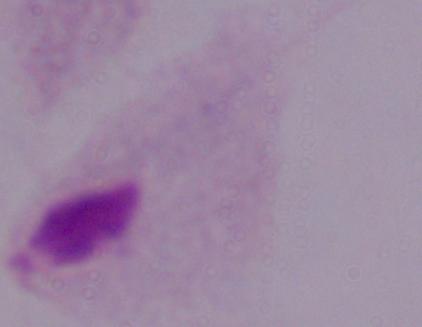

A trichomonad is seen. Photomicrograph. Captured at 1000x magnification.